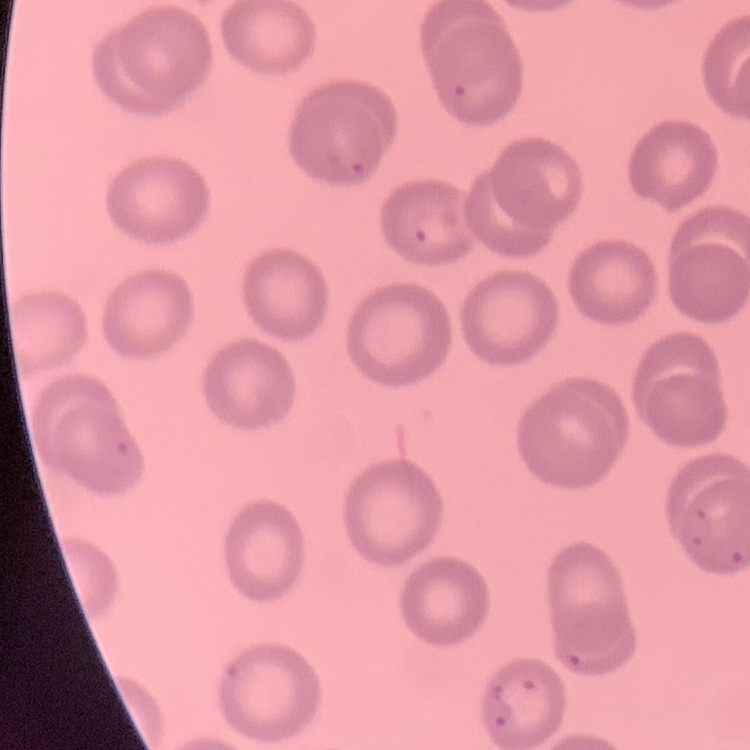

Summary:
  - Erythrocyte morphology: no rouleaux formation
  - Stain: Field's or Giemsa
  - Preparation: thin peripheral smear
  - Image type: square crop of a larger photomicrograph